Assess the morphology of the red blood cells.
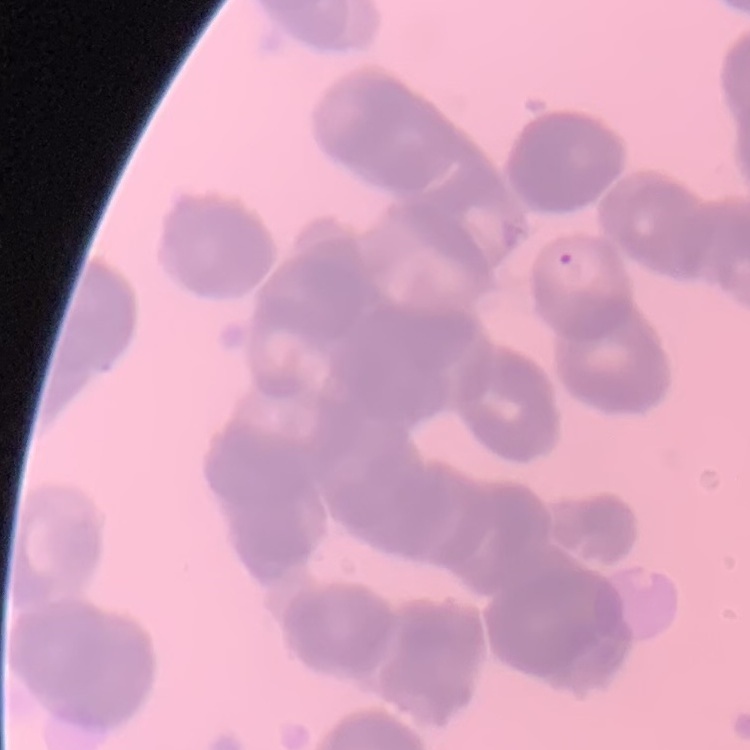
Rouleaux formation.

Summary:
  - Image type: one tile cut from a larger photomicrograph
  - Preparation: thin peripheral smear
  - Stain: Field's or Giemsa